Comment on the morphology of the red blood cells.
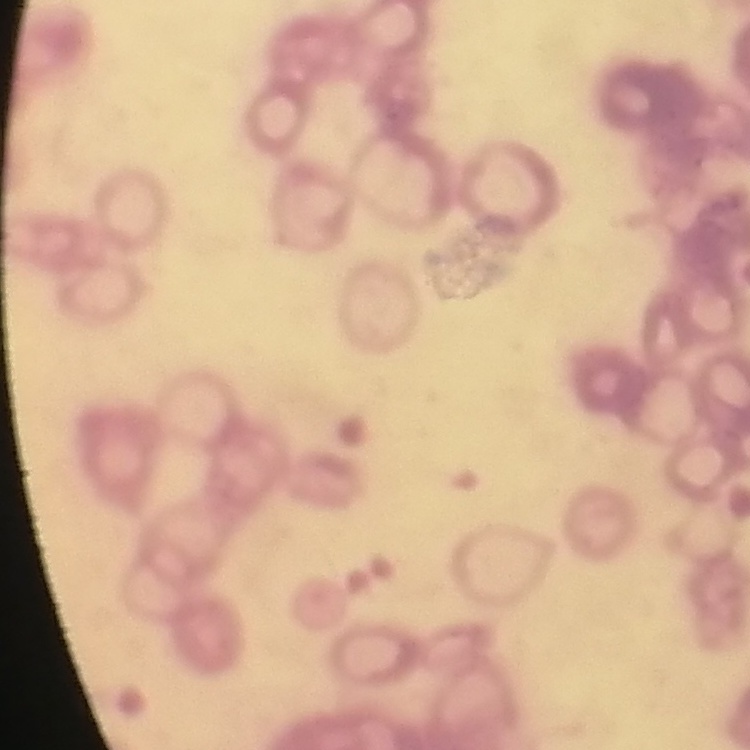
They show rouleaux formation.

Summary:
  - Image type: square crop of a larger photomicrograph
  - Stain: Field's or Giemsa
  - Preparation: thin peripheral smear